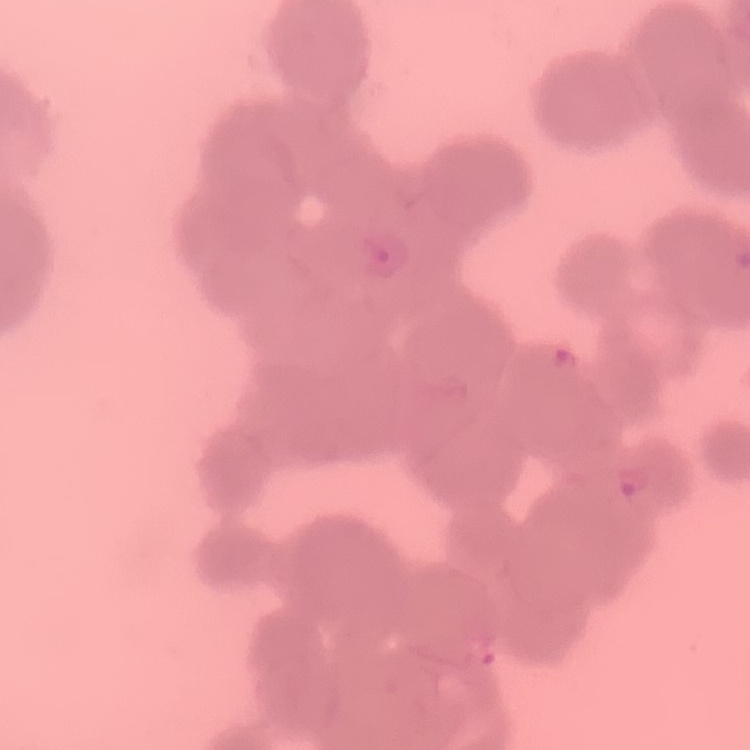

Summary:
  - Erythrocyte morphology: rouleaux formation
  - Stain: Field's or Giemsa
  - Image type: square crop of a larger photomicrograph
  - Preparation: thin blood film